Locate every blood parasite and identify its species.
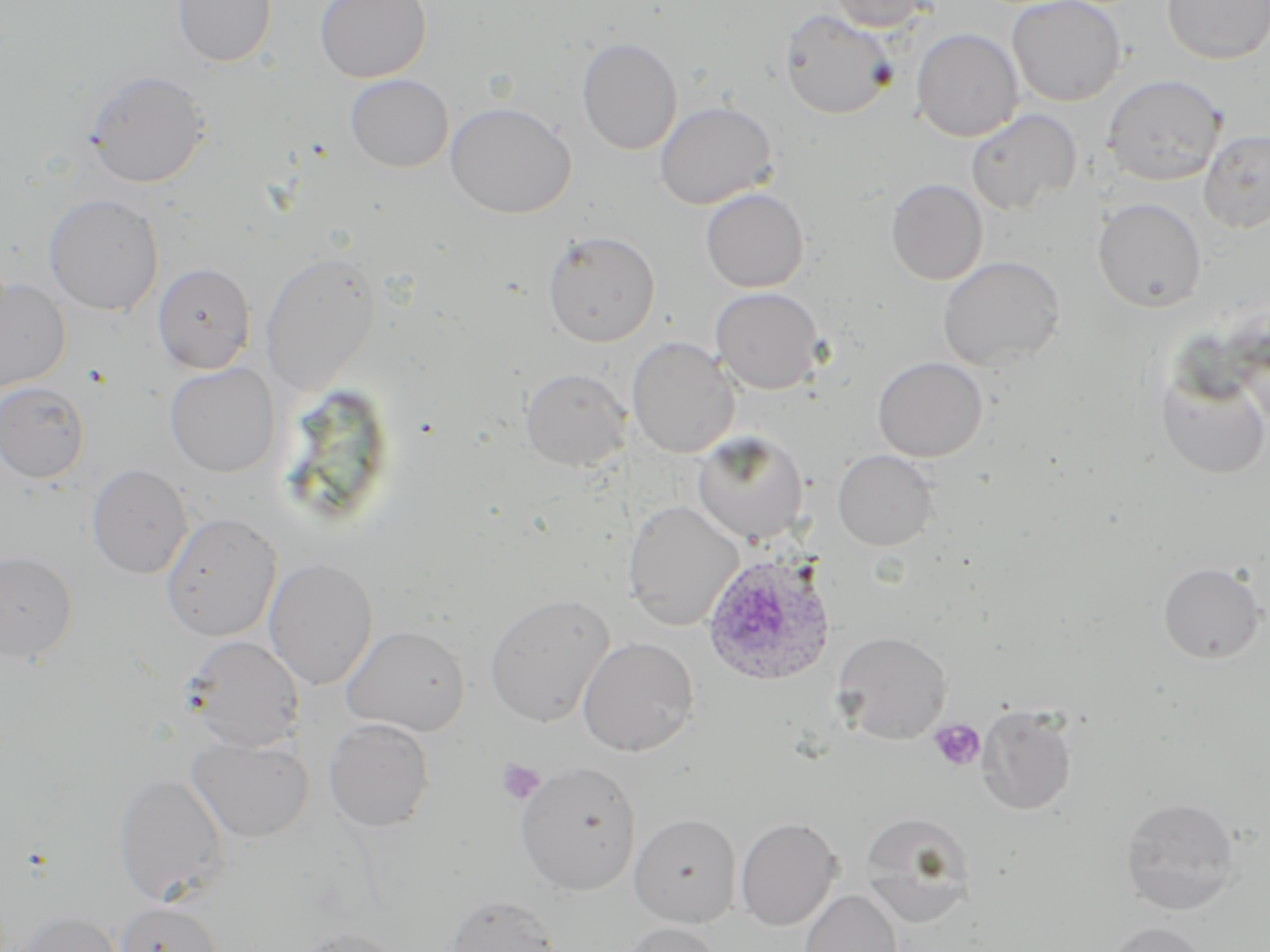
Approximate bounding boxes as (x1,y1)-(x2,y2) corner pairs in pixels.
Plasmodium ovale-infected red blood cells: (702,551)-(837,687).
No Plasmodium falciparum, Plasmodium malariae, Plasmodium vivax, Babesia divergens, or Trypanosoma brucei observed.

Platelet locations: (928,718)-(986,772), (496,758)-(545,805). Uninfected red blood cell locations: (172,0)-(278,67), (314,0)-(431,82), (827,0)-(936,32), (1006,0)-(1126,106), (1162,0)-(1270,64), (779,9)-(898,120), (911,28)-(1024,142), (576,37)-(682,155), (84,69)-(212,188), (345,73)-(453,172), (1102,74)-(1227,186), (654,101)-(778,209), (445,102)-(576,218), (965,108)-(1083,214), (1199,128)-(1270,233), (885,178)-(988,285), (700,188)-(809,292), (44,194)-(164,316), (1092,197)-(1207,312), (542,230)-(661,346), (260,251)-(381,397), (937,255)-(1067,372), (153,263)-(255,374), (0,276)-(71,393), (710,287)-(826,394), (626,337)-(740,458), (872,356)-(988,462), (164,363)-(280,477), (1156,365)-(1270,480), (521,367)-(630,471), (1,380)-(91,483), (691,432)-(808,544), (833,449)-(938,551), (87,463)-(193,579), (622,498)-(743,631), (160,511)-(282,642), (0,550)-(79,663), (263,557)-(377,690), (1157,562)-(1267,664), (484,593)-(615,728), (342,624)-(472,735), (832,630)-(952,744), (184,635)-(305,752), (578,636)-(699,756), (976,705)-(1077,815), (324,718)-(435,832), (187,735)-(315,843), (515,761)-(642,895), (114,771)-(230,906), (1119,796)-(1243,915), (859,812)-(977,926), (629,813)-(741,928), (736,817)-(841,931), (800,889)-(903,952), (444,893)-(562,952), (115,901)-(224,952), (16,910)-(126,952), (1104,921)-(1211,952), (617,922)-(723,952), (286,927)-(410,952). Slide-level diagnosis: Plasmodium ovale. One field of a larger specimen. Thin blood smear. Light microscopy. May-Grünwald-Giemsa-stained preparation. Image is 1270×952 pixels. 1000x magnification.